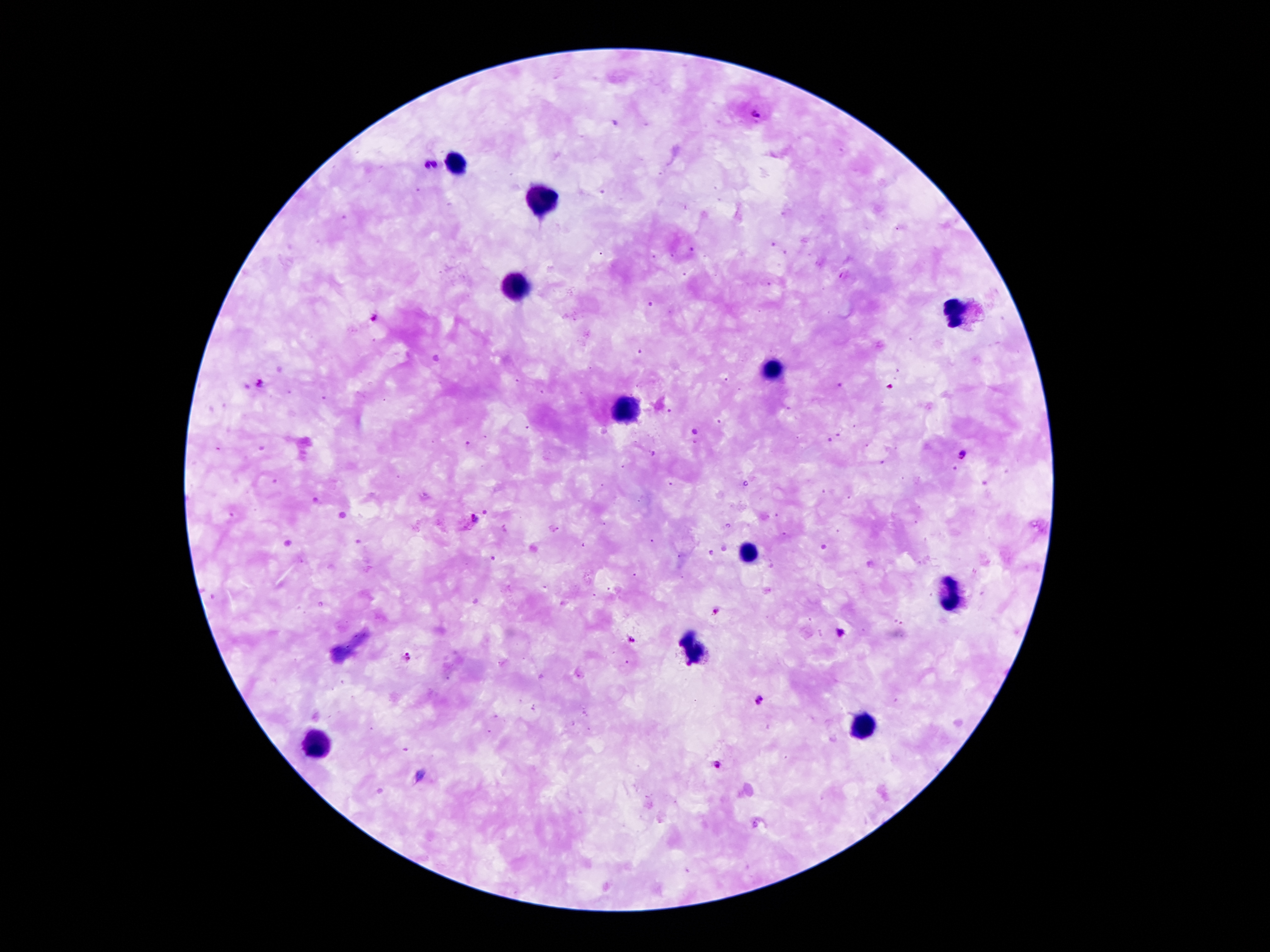

Approximate centers as {x, y} in pixels.
Summary:
  - Malaria parasite locations: {756, 115}, {425, 165}, {435, 165}, {375, 317}, {258, 383}, {963, 456}, {476, 520}, {715, 611}, {841, 633}, {631, 641}, {406, 657}, {761, 700}, {718, 764}
  - Leukocyte locations: {456, 162}, {538, 201}, {513, 285}, {956, 312}, {773, 371}, {626, 409}, {748, 550}, {956, 596}, {694, 648}, {866, 726}, {320, 743}
  - Image size: 1270×952 pixels
  - Capture: smartphone through the microscope eyepiece
  - Stain: Giemsa
  - Preparation: thick blood film
  - Field of view: single
  - Magnification: 100x
  - Patient malaria status: positive for Plasmodium falciparum